Report the malaria status of this cell.
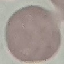

It is uninfected.

capture: smartphone camera at the microscope eyepiece
preparation: thin blood film
stain: Giemsa
image_type: cell patch, automatically extracted from a larger field of view and resized to 64 × 64 pixels